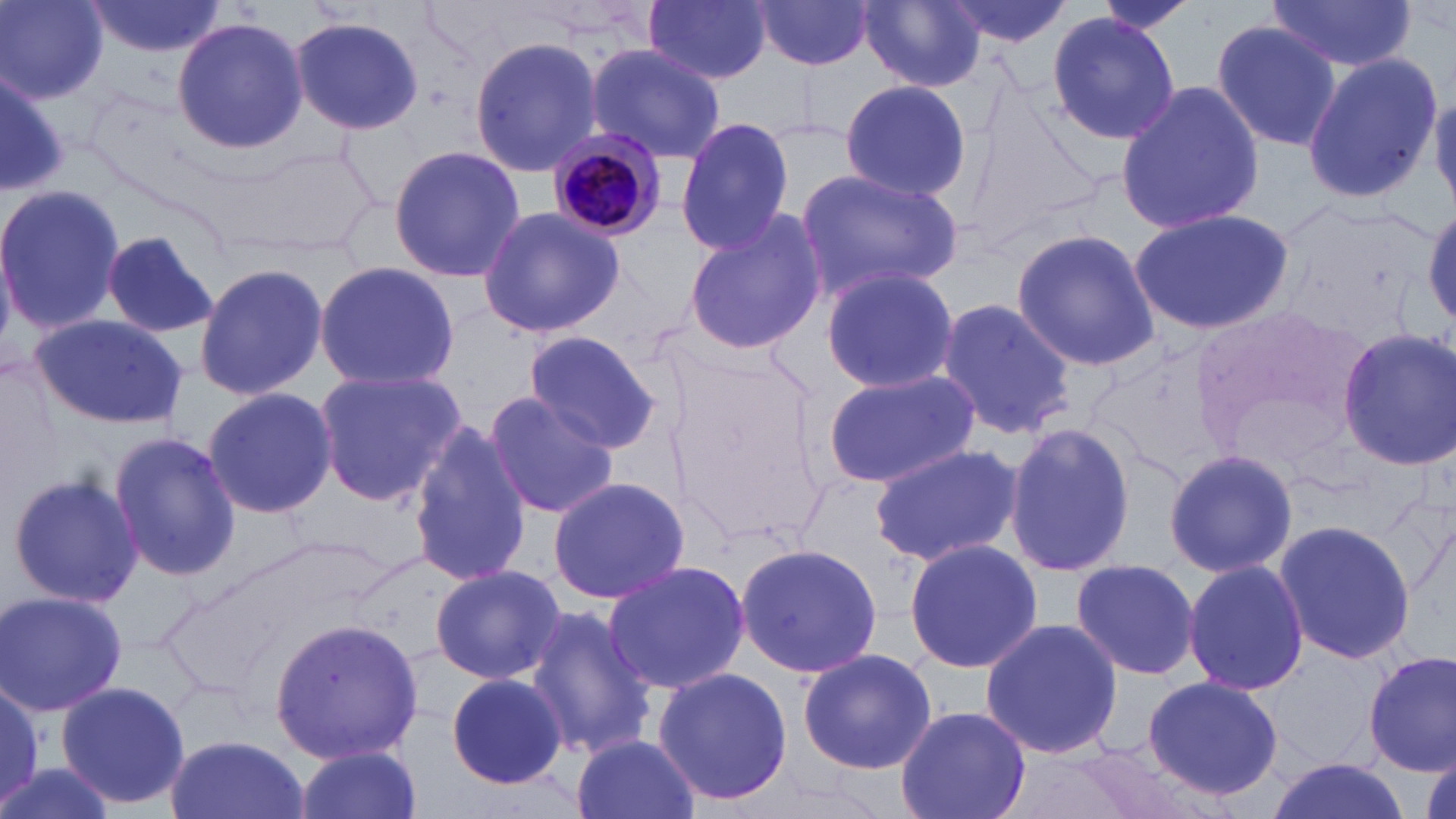

Summary:
  - Coordinate format: approximate bounding boxes as (x1,y1)-(x2,y2) corner pairs in pixels
  - Uninfected red blood cell locations: (1,0)-(108,103), (644,0)-(773,85), (941,0)-(1070,49), (1080,0)-(1208,33), (1265,0)-(1420,73), (83,1)-(226,57), (750,1)-(876,71), (855,2)-(991,91), (1047,10)-(1180,143), (290,15)-(424,136), (172,16)-(307,154), (1210,20)-(1342,154), (469,36)-(602,178), (585,42)-(728,165), (1301,52)-(1441,206), (0,65)-(66,200), (838,79)-(972,202), (1115,81)-(1264,238), (1430,87)-(1456,212), (676,117)-(796,255), (387,144)-(524,285), (795,167)-(961,301), (0,184)-(125,333), (1424,204)-(1456,330), (476,206)-(626,339), (1130,207)-(1296,336), (681,211)-(825,357), (1010,230)-(1161,372), (98,231)-(221,342), (193,260)-(330,401), (314,261)-(460,391), (819,267)-(958,392), (934,298)-(1076,438), (27,314)-(187,428), (1336,327)-(1456,469), (522,331)-(662,454), (1,354)-(60,493), (311,368)-(467,506), (821,368)-(981,490), (203,388)-(337,516), (482,391)-(621,519), (1004,422)-(1132,577), (407,423)-(534,587), (108,430)-(240,583), (870,443)-(1023,566), (1161,447)-(1298,578), (7,471)-(144,610), (546,475)-(692,605), (1273,517)-(1418,668), (904,537)-(1042,674), (734,542)-(883,679), (604,559)-(749,694), (1069,559)-(1202,684), (1182,559)-(1309,697), (429,563)-(564,683), (0,589)-(128,717), (523,605)-(659,762), (268,618)-(424,765), (979,618)-(1123,760), (797,647)-(937,775), (1269,649)-(1391,769), (1363,652)-(1455,777), (654,667)-(794,808), (444,672)-(571,790), (1142,674)-(1284,801), (1,679)-(46,812), (55,679)-(191,813), (896,705)-(1030,819), (164,733)-(310,819), (570,733)-(700,819), (289,745)-(421,819), (0,758)-(119,819), (1262,758)-(1410,819)
  - Plasmodium malariae-infected red blood cell locations: (545,129)-(669,242)
  - Slide-level diagnosis: Plasmodium malariae
  - Field of view: single
  - Magnification: 1000x
  - Preparation: thin blood film
  - Stain: May-Grünwald-Giemsa
  - Image size: 1456×819 pixels
  - Modality: optical microscopy